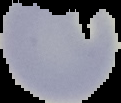
Summary:
  - Preparation: thin blood smear
  - Image size: 121×103 pixels
  - Malaria status: uninfected
  - Image type: segmented cell region on a black background